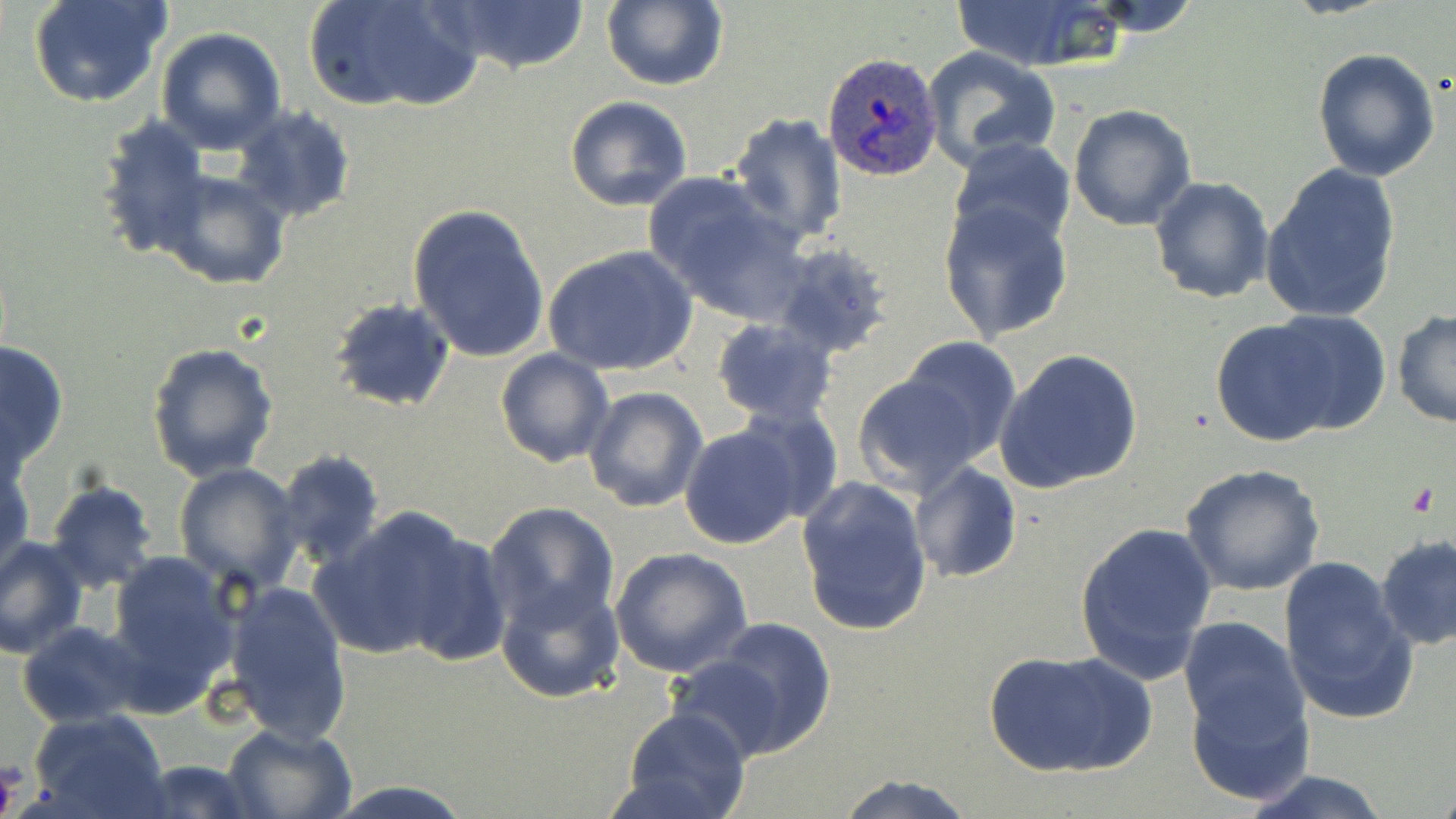

{
  "slide_level_diagnosis": "Plasmodium ovale",
  "image_size": "1456×819 pixels",
  "magnification": "1000x",
  "preparation": "thin blood smear",
  "field_of_view": "one of a larger specimen",
  "uninfected_red_blood_cell_locations": "approximate bounding boxes as (x1, y1, x2, y2) in pixels: (28, 0, 171, 109), (301, 0, 479, 113), (949, 0, 1131, 72), (438, 1, 589, 78), (599, 1, 728, 90), (157, 27, 286, 155), (921, 46, 1061, 171), (1311, 46, 1441, 181), (565, 94, 694, 212), (1068, 103, 1198, 231), (230, 106, 356, 224), (727, 113, 848, 245), (95, 114, 210, 260), (948, 138, 1076, 253), (1260, 163, 1401, 324), (153, 168, 291, 291), (1150, 175, 1274, 304), (647, 177, 810, 324), (407, 201, 552, 364), (939, 203, 1075, 344), (771, 242, 897, 361), (543, 245, 698, 377), (328, 297, 457, 413), (1261, 308, 1395, 438), (1391, 310, 1455, 430), (710, 319, 838, 426), (1209, 319, 1353, 447), (901, 338, 1024, 462), (0, 340, 71, 471), (145, 342, 279, 483), (495, 348, 614, 467), (994, 348, 1143, 494), (850, 371, 988, 498), (583, 386, 708, 514), (736, 403, 842, 523), (678, 423, 804, 549), (1, 446, 34, 573), (276, 450, 386, 571), (911, 462, 1021, 583), (1180, 462, 1325, 596), (175, 463, 304, 594), (796, 473, 934, 637), (45, 479, 159, 595), (484, 502, 620, 632), (316, 507, 476, 660), (1074, 520, 1218, 685), (392, 528, 514, 664), (1376, 534, 1456, 652), (0, 536, 88, 659), (609, 548, 753, 679), (103, 549, 241, 707), (1278, 554, 1418, 726), (496, 579, 624, 703), (220, 581, 353, 745), (704, 616, 837, 756), (1176, 617, 1309, 748), (19, 621, 150, 729), (981, 646, 1157, 780), (663, 652, 801, 764), (1182, 680, 1309, 807), (620, 707, 752, 819), (28, 709, 172, 818), (220, 723, 357, 819), (137, 758, 259, 818), (1238, 771, 1395, 819), (829, 772, 978, 818), (319, 779, 481, 819)",
  "modality": "light microscopy",
  "platelet_locations": "approximate bounding boxes as (x1, y1, x2, y2) in pixels: (0, 764, 21, 817)",
  "plasmodium_ovale_infected_red_blood_cell_locations": "approximate bounding boxes as (x1, y1, x2, y2) in pixels: (822, 52, 941, 177)",
  "stain": "May-Grünwald-Giemsa"
}